Identify the parasite.
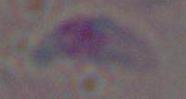

Toxoplasma gondii.

modality: photomicrograph
magnification: 1000x